Identify the cell.
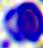
A leukocyte.

400x magnification. Photomicrograph.